Give the position of every leukocyte visible.
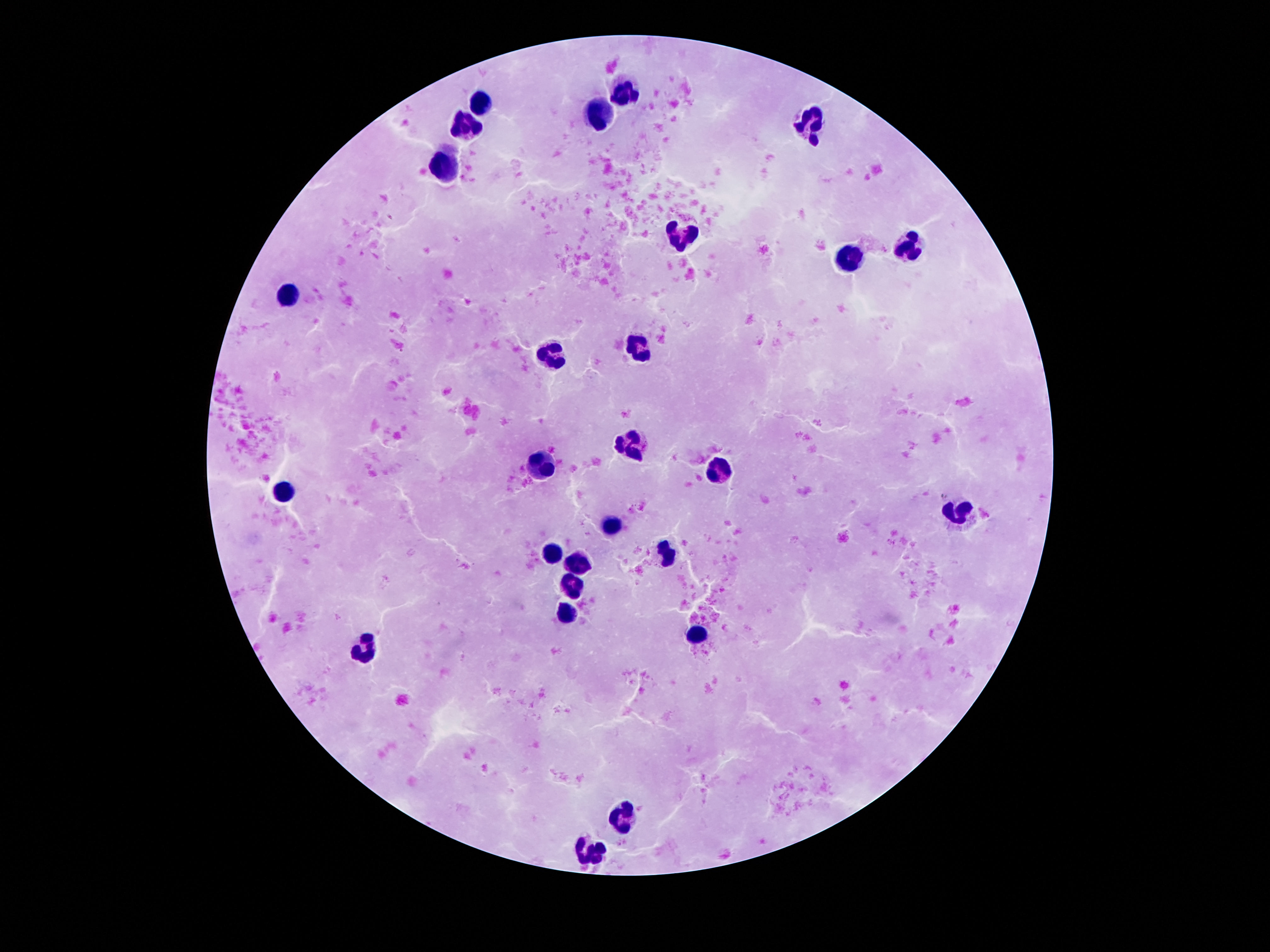
Approximate centers as (x, y) in pixels.
Leukocytes: (624, 93), (483, 107), (600, 117), (811, 124), (466, 125), (445, 166), (682, 234), (910, 245), (854, 260), (285, 298), (638, 347), (552, 356), (634, 445), (540, 463), (727, 469), (956, 512), (610, 522), (547, 550), (664, 550), (577, 563), (570, 588), (567, 616), (699, 635), (364, 647), (623, 812), (592, 851).

preparation = thick blood smear
capture = smartphone camera through the microscope eyepiece
stain = Giemsa
image size = 1270×952 pixels
field of view = one from this slide
patient malaria status = uninfected
magnification = 100x